Classify this cell by malaria status.
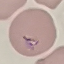

Parasitized.

Summary:
  - Image type: automatically extracted cell patch, resized to 64 × 64 pixels
  - Capture: smartphone through the microscope eyepiece
  - Preparation: thin blood film
  - Stain: Giemsa